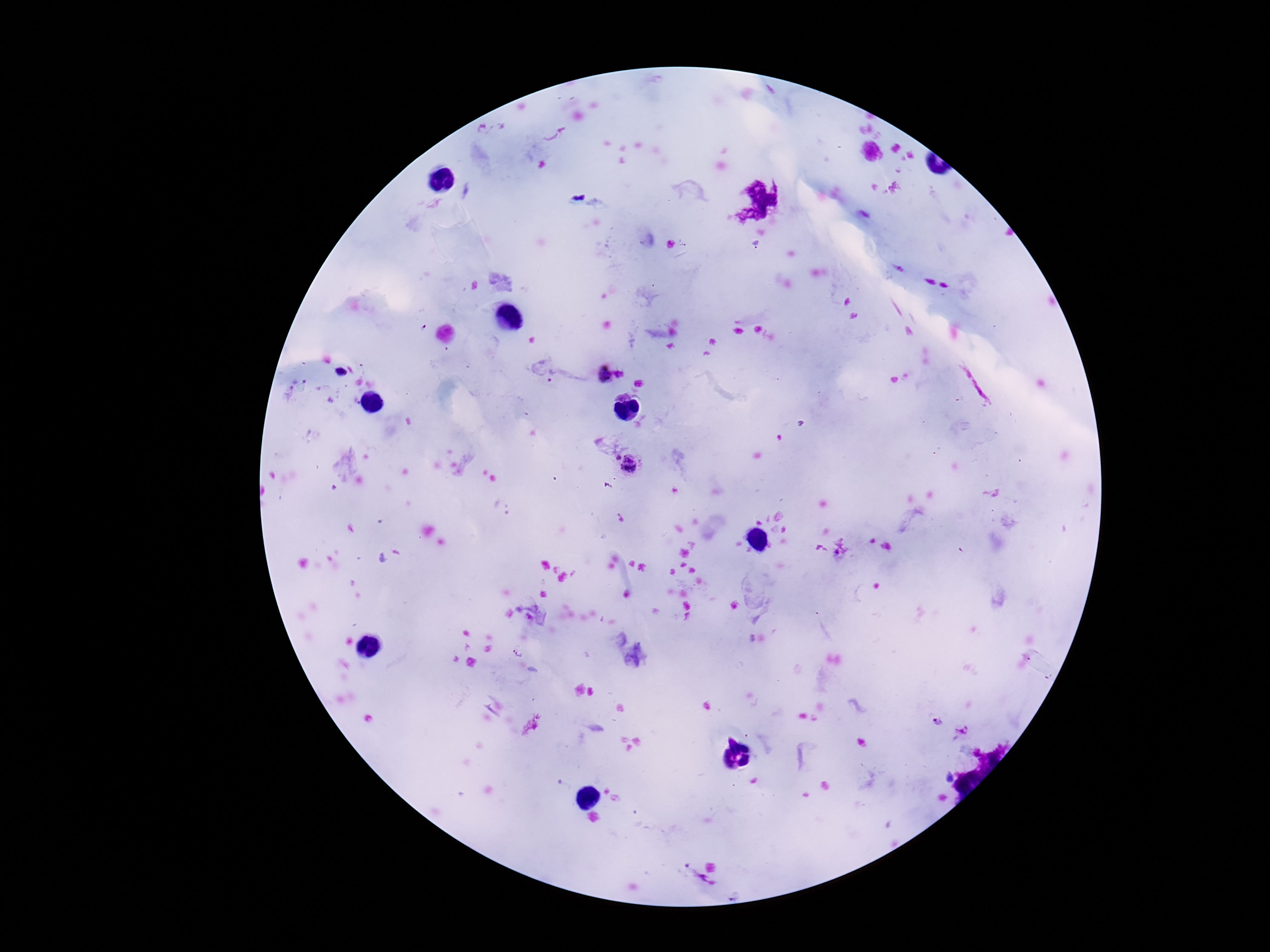

preparation = thick peripheral-blood smear
stain = Giemsa
magnification = 100x
capture = smartphone camera through the microscope eyepiece
Plasmodium parasite locations = approximate centers as (x, y) in pixels: (622, 374), (604, 375), (616, 457), (632, 466)
field of view = single
image size = 1270×952 pixels
patient malaria status = positive